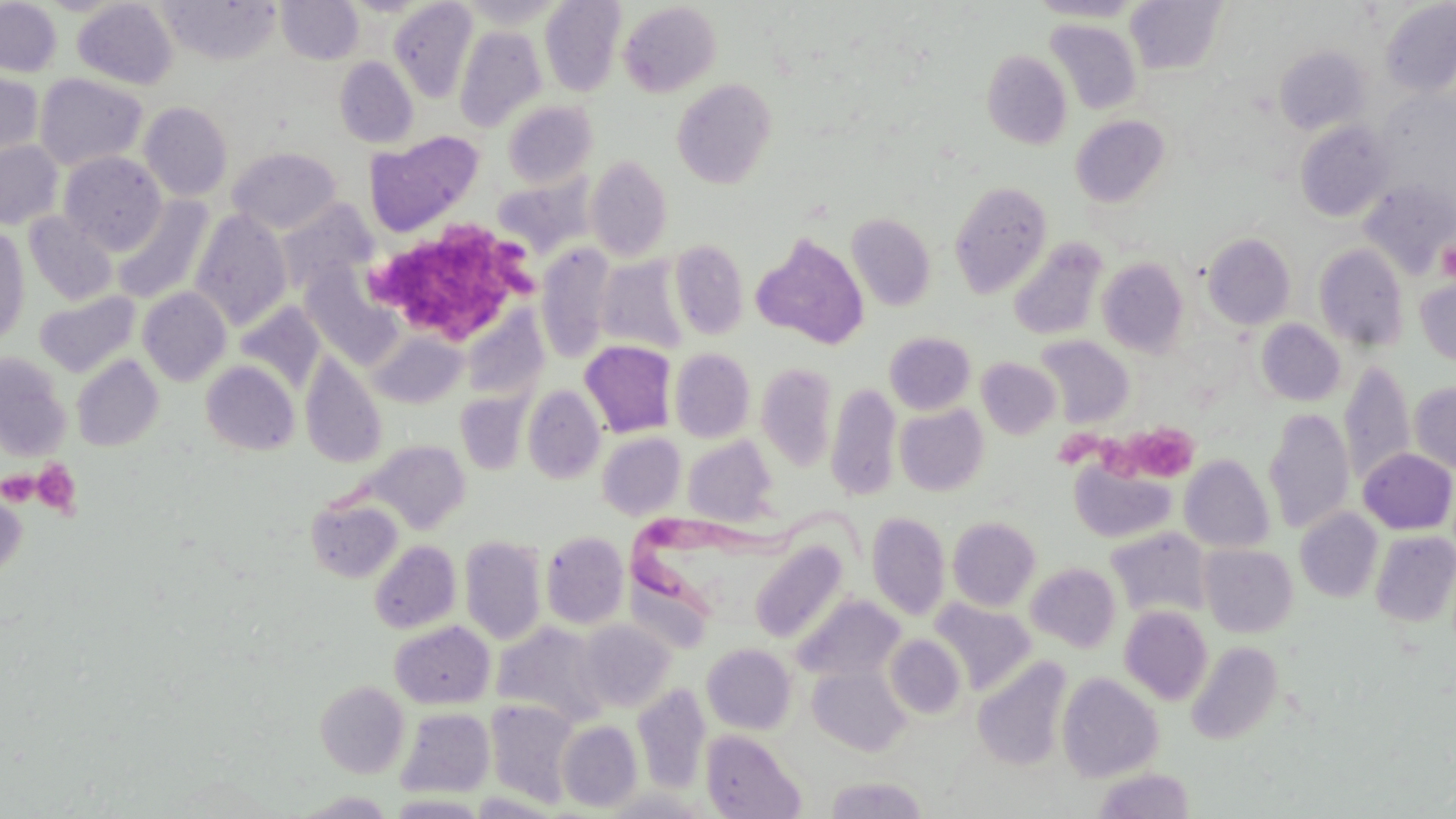

Summary:
  - Coordinate format: approximate bounding boxes as [x1, y1, x2, y2] in pixels
  - Trypanosoma brucei locations: [633, 503, 878, 621]
  - Platelet locations: [373, 212, 533, 343], [1437, 237, 1456, 283], [1129, 424, 1200, 485], [1060, 432, 1099, 467], [1095, 434, 1144, 485], [32, 458, 82, 517], [1, 470, 41, 505]
  - Uninfected red blood cell locations: [159, 0, 281, 65], [276, 0, 363, 65], [456, 0, 565, 28], [1027, 0, 1144, 22], [1125, 0, 1228, 75], [0, 1, 62, 77], [73, 1, 178, 89], [389, 1, 477, 103], [540, 1, 625, 96], [1380, 1, 1456, 99], [618, 2, 722, 97], [1046, 19, 1141, 115], [455, 25, 547, 132], [1274, 45, 1371, 135], [982, 50, 1072, 149], [335, 56, 419, 148], [0, 71, 43, 162], [34, 73, 148, 171], [673, 78, 778, 188], [1377, 91, 1455, 197], [503, 101, 597, 188], [139, 102, 233, 201], [1070, 115, 1170, 207], [1295, 120, 1395, 222], [364, 129, 484, 238], [0, 140, 63, 229], [227, 146, 341, 234], [58, 151, 167, 254], [586, 155, 673, 261], [493, 175, 593, 257], [1359, 178, 1456, 279], [949, 180, 1053, 298], [113, 196, 214, 305], [277, 199, 375, 293], [190, 209, 293, 330], [23, 212, 118, 306], [846, 213, 936, 311], [0, 226, 30, 346], [1203, 232, 1296, 330], [752, 233, 869, 349], [1009, 238, 1108, 341], [670, 239, 749, 340], [1314, 243, 1409, 351], [535, 244, 616, 361], [595, 255, 689, 355], [1097, 257, 1189, 357], [1415, 276, 1456, 369], [138, 287, 231, 385], [35, 291, 140, 376], [235, 301, 326, 394], [461, 308, 549, 403], [1256, 319, 1345, 405], [369, 330, 467, 408], [884, 332, 975, 414], [1035, 335, 1134, 428], [579, 340, 677, 438], [670, 348, 755, 442], [300, 351, 387, 469], [0, 353, 72, 458], [72, 355, 163, 451], [976, 357, 1061, 439], [201, 360, 300, 455], [1339, 360, 1416, 490], [756, 362, 837, 473], [826, 382, 901, 500], [1410, 382, 1456, 475], [523, 384, 605, 484], [455, 391, 532, 475], [895, 404, 989, 496], [1263, 408, 1355, 535], [598, 432, 686, 520], [683, 436, 778, 525], [363, 440, 470, 534], [1358, 448, 1456, 534], [1179, 455, 1275, 553], [1069, 458, 1177, 543], [0, 482, 28, 580], [306, 497, 403, 582], [1294, 508, 1383, 602], [867, 511, 950, 620], [947, 517, 1041, 610], [1106, 527, 1212, 620], [1370, 530, 1456, 627], [541, 531, 629, 629], [459, 535, 546, 644], [369, 540, 461, 633], [750, 540, 848, 642], [1199, 544, 1298, 637], [1027, 562, 1121, 652], [793, 594, 904, 682], [930, 599, 1036, 695], [1119, 605, 1213, 705], [389, 620, 495, 708], [578, 621, 675, 712], [492, 623, 608, 726], [885, 635, 966, 718], [1186, 641, 1283, 745], [702, 643, 797, 734], [973, 657, 1072, 772], [808, 665, 910, 755], [1056, 672, 1163, 782], [315, 680, 409, 777], [632, 682, 711, 794], [485, 699, 581, 807], [396, 708, 495, 798], [557, 720, 642, 811], [702, 730, 805, 818], [1094, 768, 1195, 819], [826, 775, 926, 818], [294, 792, 397, 818]
  - Slide-level diagnosis: Trypanosoma brucei
  - Magnification: 1000x
  - Image size: 1456×819 pixels
  - Field of view: single
  - Modality: light microscopy
  - Stain: May-Grünwald-Giemsa
  - Preparation: thin blood film